Locate every Plasmodium parasite.
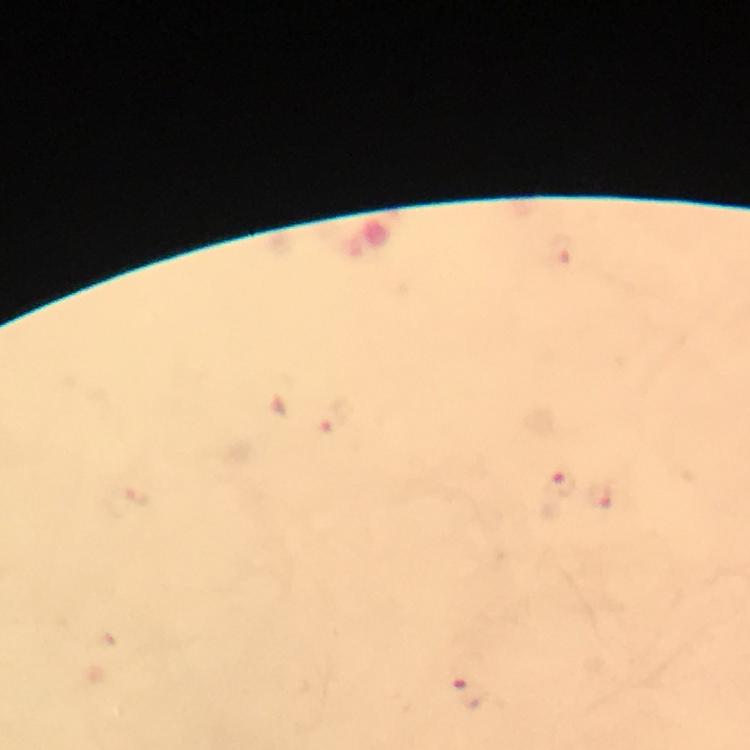

Approximate centers as (x, y) in pixels.
Plasmodium parasites: (562, 481), (598, 498), (470, 691).

From a diagnostic examination for malaria. Image is 750×750 pixels. At 100x magnification. Thick smear. Photographed through the microscope with a smartphone camera. Immersion oil applied. Cropped region of a single field of view. Giemsa stain.